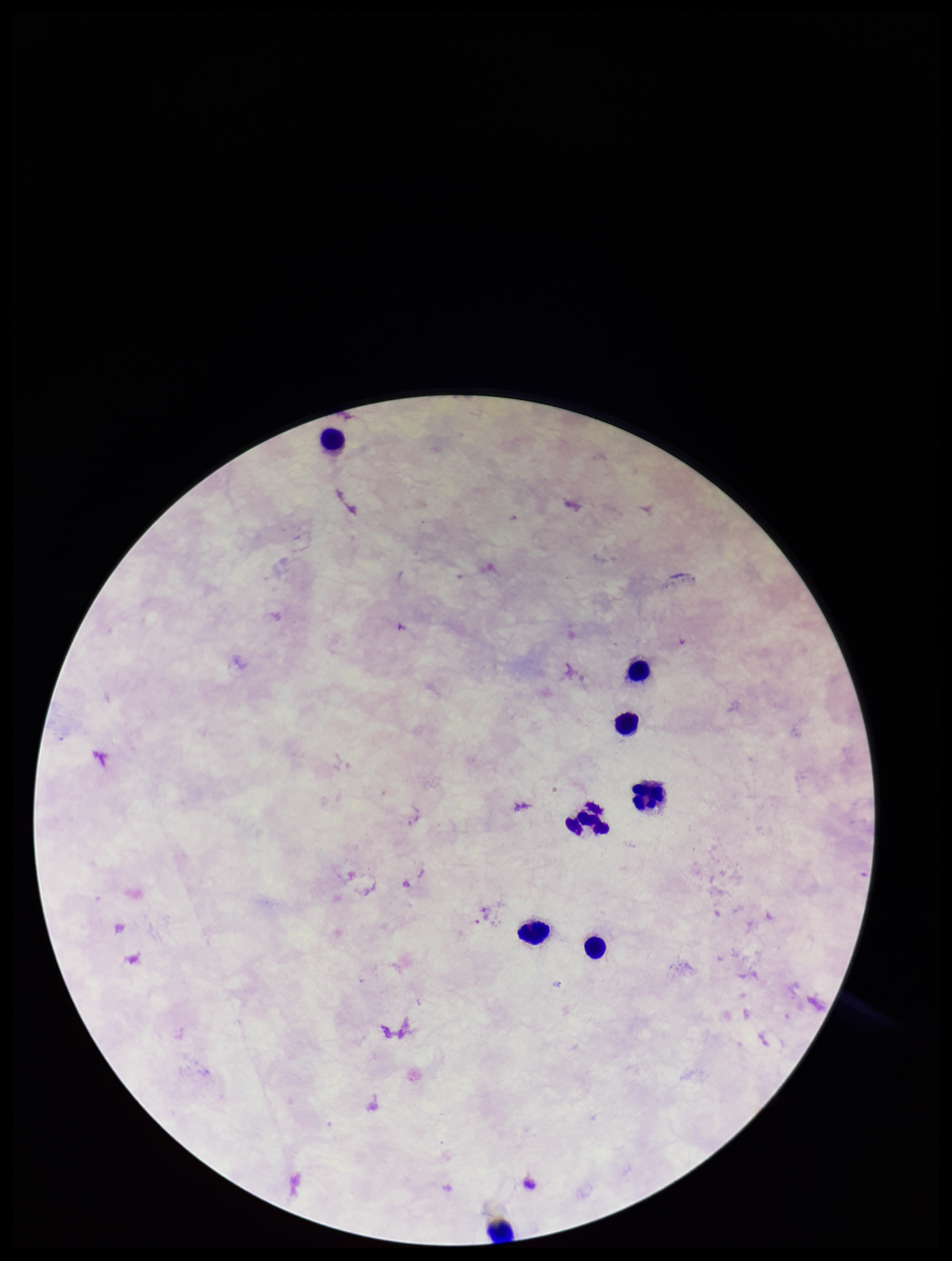

Summary:
  - Preparation: thick
  - Field of view: one from this slide
  - Plasmodium parasites: none detected
  - Image size: 952×1261 pixels
  - Patient malaria status: negative
  - Capture: smartphone photograph through the microscope eyepiece
  - Stain: Giemsa
  - Parasite count: 0
  - Leukocyte count: 8